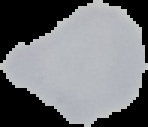

Summary:
  - Image type: segmented cell region with the area outside set to black
  - Preparation: thin blood film
  - Malaria status: uninfected
  - Image size: 148×127 pixels